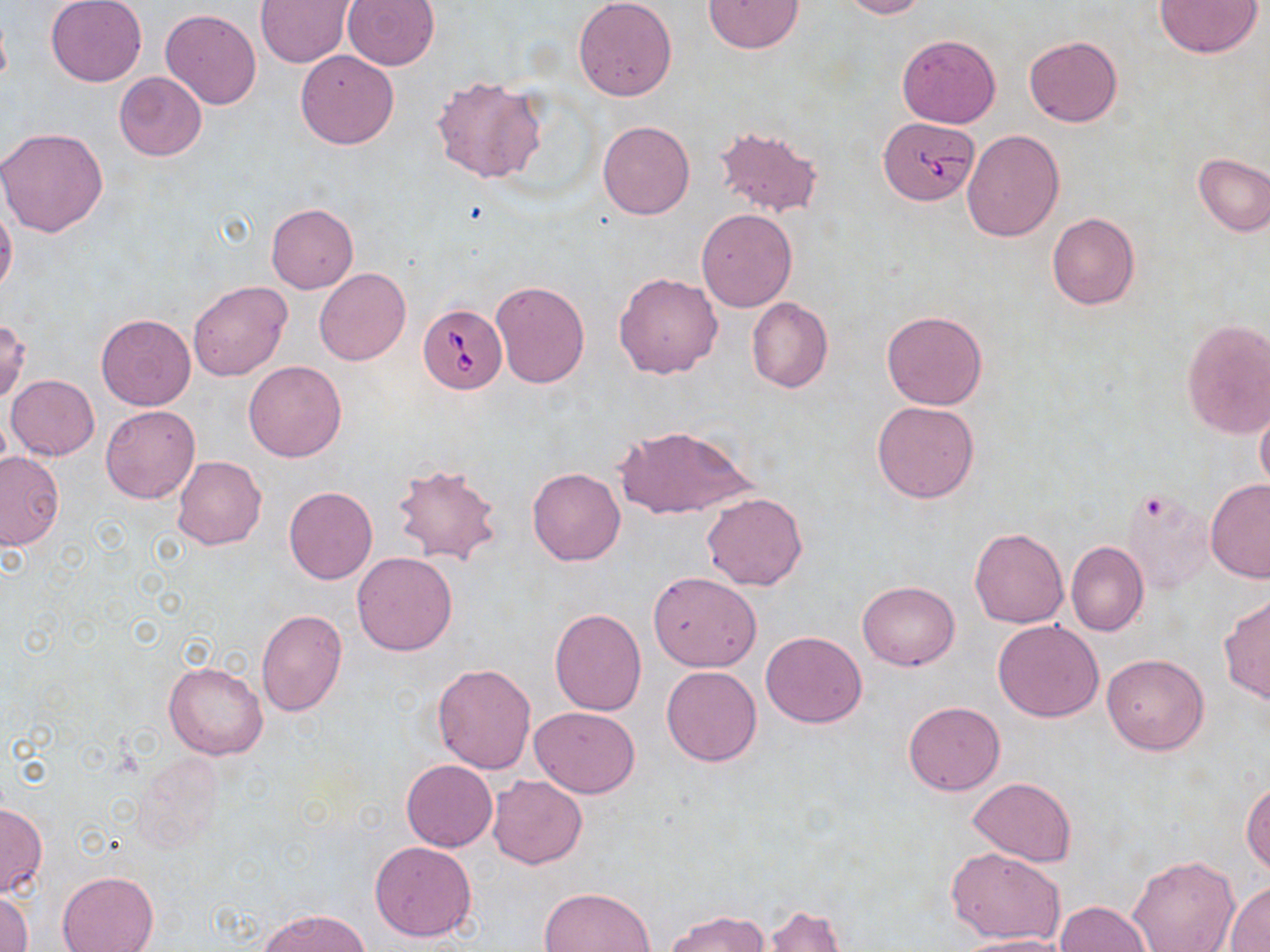 Approximate bounding boxes as [x1, y1, x2, y2] in pixels. Babesia divergens-infected red blood cell locations: [877, 118, 979, 207], [418, 303, 507, 393]. Uninfected red blood cell locations: [255, 0, 355, 67], [341, 0, 440, 69], [573, 0, 677, 101], [837, 0, 928, 19], [47, 1, 147, 86], [703, 1, 803, 53], [1154, 1, 1262, 56], [160, 9, 261, 110], [896, 34, 1000, 129], [1024, 35, 1122, 127], [295, 49, 400, 150], [113, 71, 207, 161], [431, 76, 546, 184], [597, 120, 694, 219], [712, 123, 823, 217], [0, 127, 108, 237], [961, 128, 1064, 242], [1193, 152, 1270, 237], [0, 204, 18, 299], [265, 204, 359, 293], [696, 208, 798, 312], [1047, 213, 1140, 310], [314, 268, 410, 365], [614, 271, 723, 378], [187, 280, 292, 381], [490, 281, 590, 388], [747, 298, 833, 392], [881, 310, 988, 410], [96, 313, 196, 410], [0, 319, 30, 403], [1181, 319, 1270, 438], [243, 360, 347, 462], [6, 374, 99, 460], [872, 400, 980, 503], [1256, 404, 1270, 496], [101, 405, 200, 503], [615, 426, 753, 519], [0, 451, 64, 549], [172, 456, 266, 550], [390, 460, 503, 564], [527, 467, 625, 566], [1205, 479, 1270, 582], [284, 487, 377, 584], [1122, 488, 1214, 592], [703, 492, 808, 590], [970, 527, 1068, 629], [1066, 541, 1149, 636], [352, 552, 458, 656], [648, 572, 761, 672], [857, 581, 961, 671], [1219, 593, 1269, 704], [549, 609, 647, 715], [256, 610, 347, 716], [993, 619, 1105, 722], [761, 631, 867, 727], [1102, 652, 1208, 755], [164, 659, 269, 760], [431, 663, 537, 773], [662, 666, 762, 767], [903, 701, 1004, 795], [530, 705, 638, 798], [135, 754, 226, 854], [401, 759, 497, 851], [486, 774, 587, 869], [968, 777, 1077, 865], [1242, 779, 1270, 874], [0, 803, 47, 897], [369, 841, 477, 942], [947, 847, 1065, 943], [1127, 852, 1240, 951], [58, 871, 158, 952], [1225, 883, 1270, 950], [539, 888, 654, 952], [0, 889, 33, 952], [1057, 901, 1151, 952], [759, 905, 847, 952], [261, 908, 368, 951], [666, 910, 770, 951], [955, 935, 1066, 952]. Slide-level diagnosis: Babesia divergens. Optical microscopy. Image is 1270×952 pixels. Captured at 1000x magnification. Thin blood smear. May-Grünwald-Giemsa-stained preparation. One field of a larger specimen.